Assess this cell for malaria.
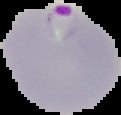
Parasitized.

From a thin blood film. Segmented cell region on a black background. Image is 121×115 pixels.